State which parasite is depicted.
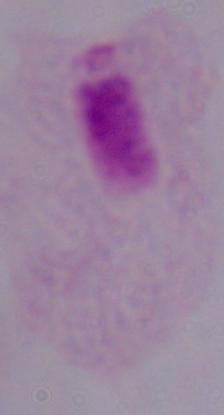

This is a trichomonad.

modality = micrograph
magnification = 1000x